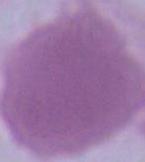

identification = red blood cell
magnification = 1000x
modality = micrograph